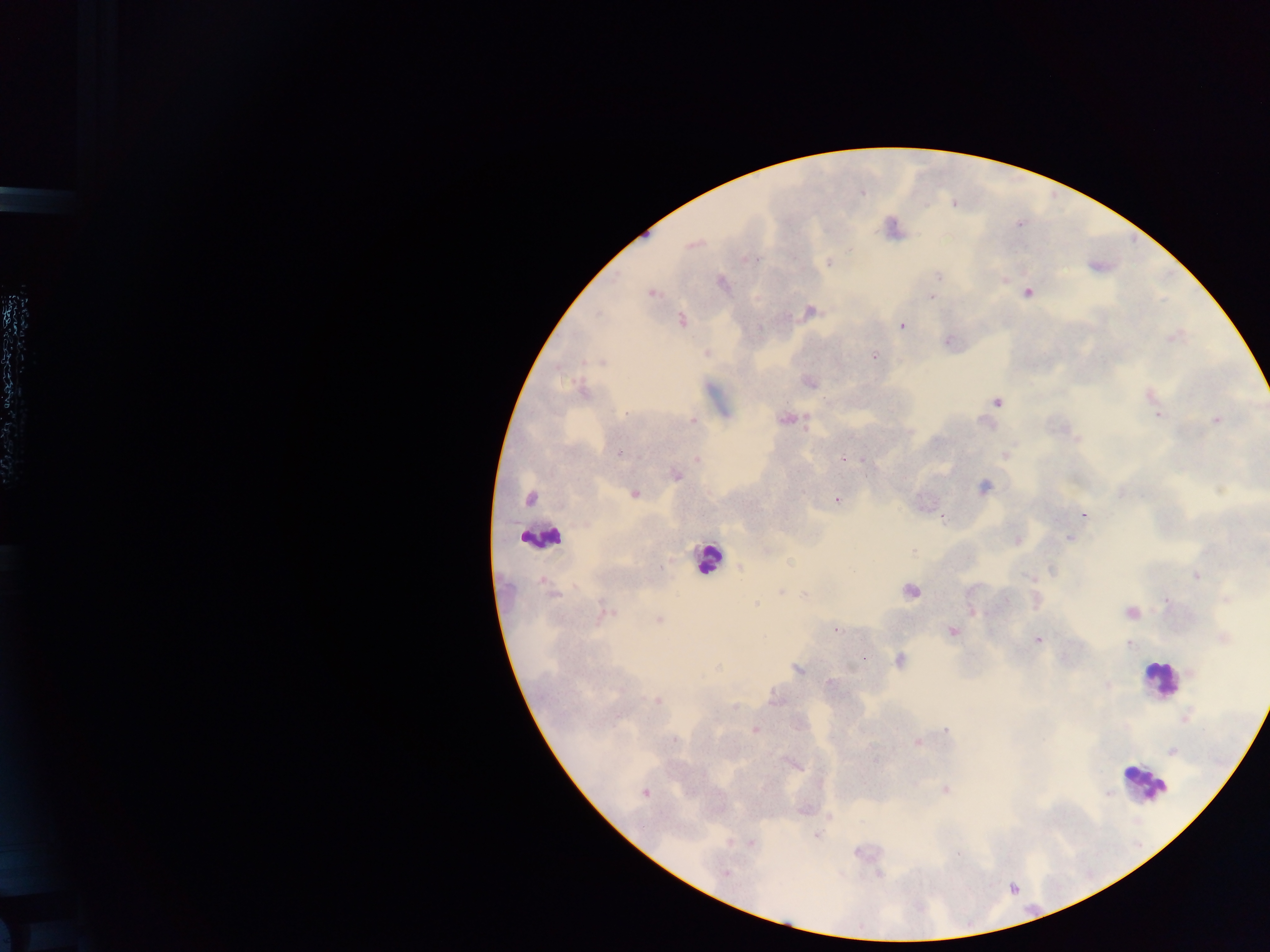

Approximate centers as {x, y} in pixels. Leukocyte locations: {542, 536}, {708, 558}, {1159, 679}, {1146, 782}. Plasmodium parasite locations: {692, 245}, {749, 259}, {829, 262}, {938, 276}, {723, 283}, {652, 293}, {1028, 293}, {932, 297}, {809, 311}, {682, 320}, {902, 326}, {1174, 338}, {948, 342}, {706, 353}, {874, 357}, {602, 362}, {809, 382}, {583, 391}, {1150, 395}, {824, 400}, {997, 402}, {626, 413}, {1157, 415}, {785, 419}, {692, 420}, {1217, 420}, {806, 425}, {619, 454}, {1005, 454}, {843, 459}, {697, 460}, {864, 462}, {676, 476}, {983, 486}, {1122, 492}, {635, 494}, {529, 499}, {836, 500}, {1083, 514}, {943, 518}, {1069, 538}, {1017, 540}, {914, 551}, {740, 569}, {1052, 571}, {1196, 575}, {1030, 578}, {911, 591}, {781, 592}, {552, 594}, {804, 595}, {1227, 598}, {1006, 601}, {1166, 601}, {755, 604}, {972, 611}, {1131, 612}, {605, 613}, {659, 620}, {835, 630}, {953, 632}, {1223, 638}, {1038, 640}, {1130, 644}, {900, 660}, {717, 667}, {797, 669}, {1192, 672}, {829, 683}, {1107, 685}, {775, 699}, {657, 700}, {734, 707}, {755, 730}, {947, 730}, {675, 739}, {918, 742}, {1172, 751}, {796, 765}, {945, 790}, {645, 793}, {1107, 794}, {817, 835}, {751, 842}, {858, 853}, {959, 854}, {726, 873}, {878, 874}. Thick blood smear. Image is 1270×952 pixels. Collected in Ghana. Photographed through a microscope with a mobile-phone camera. One field of view.